Assess the morphology of the erythrocytes.
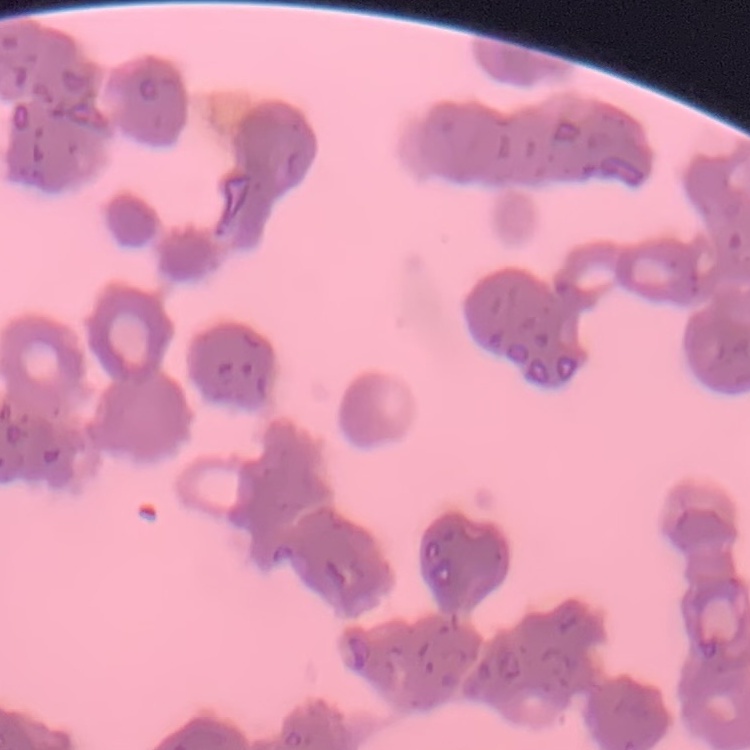
They show rouleaux formation.

One tile cut from a larger photomicrograph. Thin blood film. Stained with either Field's or Giemsa.